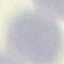

Malaria status: uninfected. Photographed with a smartphone camera at the microscope eyepiece. Thin blood smear. Giemsa-stained preparation. Automatically extracted cell patch, resized to 64 × 64 pixels.